Comment on the morphology of the red blood cells.
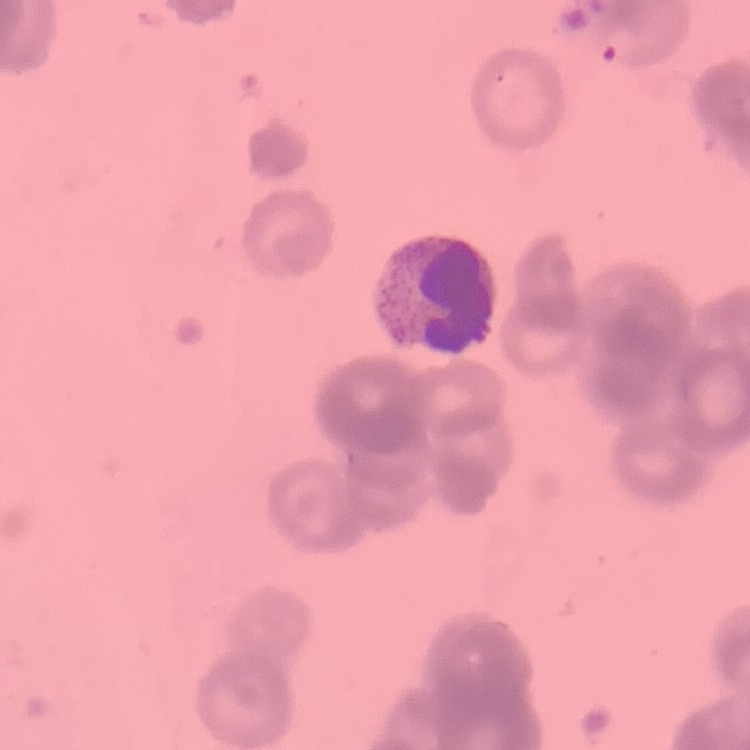

Rouleaux formation.

Summary:
  - Preparation: thin blood smear
  - Image type: square crop of a larger photomicrograph
  - Stain: Field's or Giemsa